Report the malaria status of this cell.
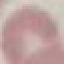

It is uninfected.

stain: Giemsa
capture: smartphone through the microscope eyepiece
preparation: thin smear
image_type: cell patch, automatically extracted from a larger field of view and resized to 64 × 64 pixels